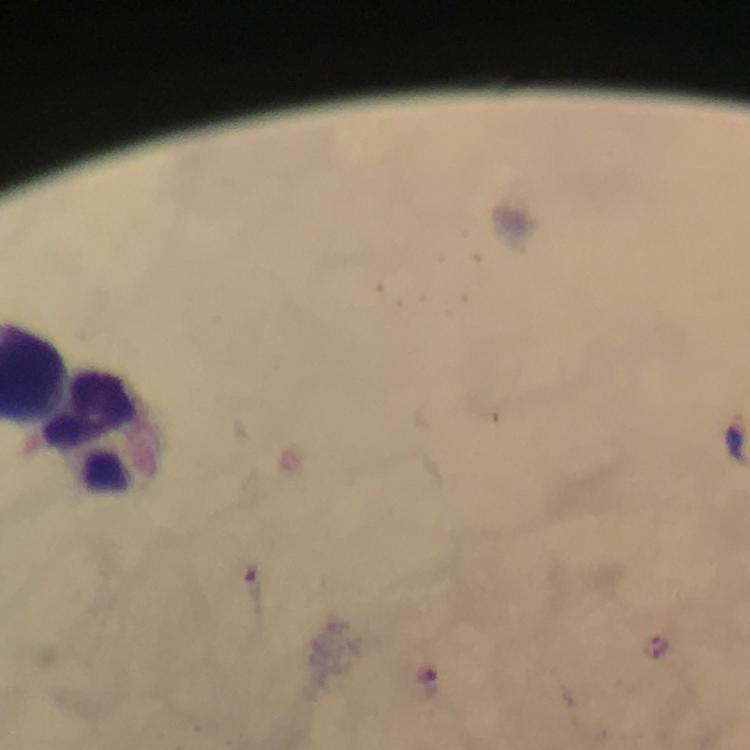
capture = smartphone camera through the microscope
leukocyte locations = approximate centers as [x, y] in pixels: [110, 427]
stain = Giemsa
immersion oil = used
magnification = 100x
cropped from = a single field of view
malaria parasite locations = approximate centers as [x, y] in pixels: [252, 592], [427, 683]
preparation = thick blood film
image size = 750×750 pixels
context = from a malaria diagnostic workup